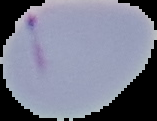

image_size: 157×121 pixels
image_type: segmented cell region on a black background
preparation: thin blood film
malaria_status: parasitized